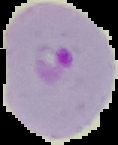

Image is 118×145 pixels. Segmented cell region on a black background. From a thin blood film. Malaria status: parasitized.